Report the malaria status of this cell.
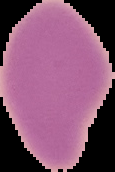

It is uninfected.

From a thin blood film. Segmented cell region on a black background. Image is 115×172 pixels.